Assess this cell for malaria.
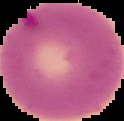

It is parasitized.

image_size: 124×121 pixels
preparation: thin blood film
image_type: segmented cell region on a black background